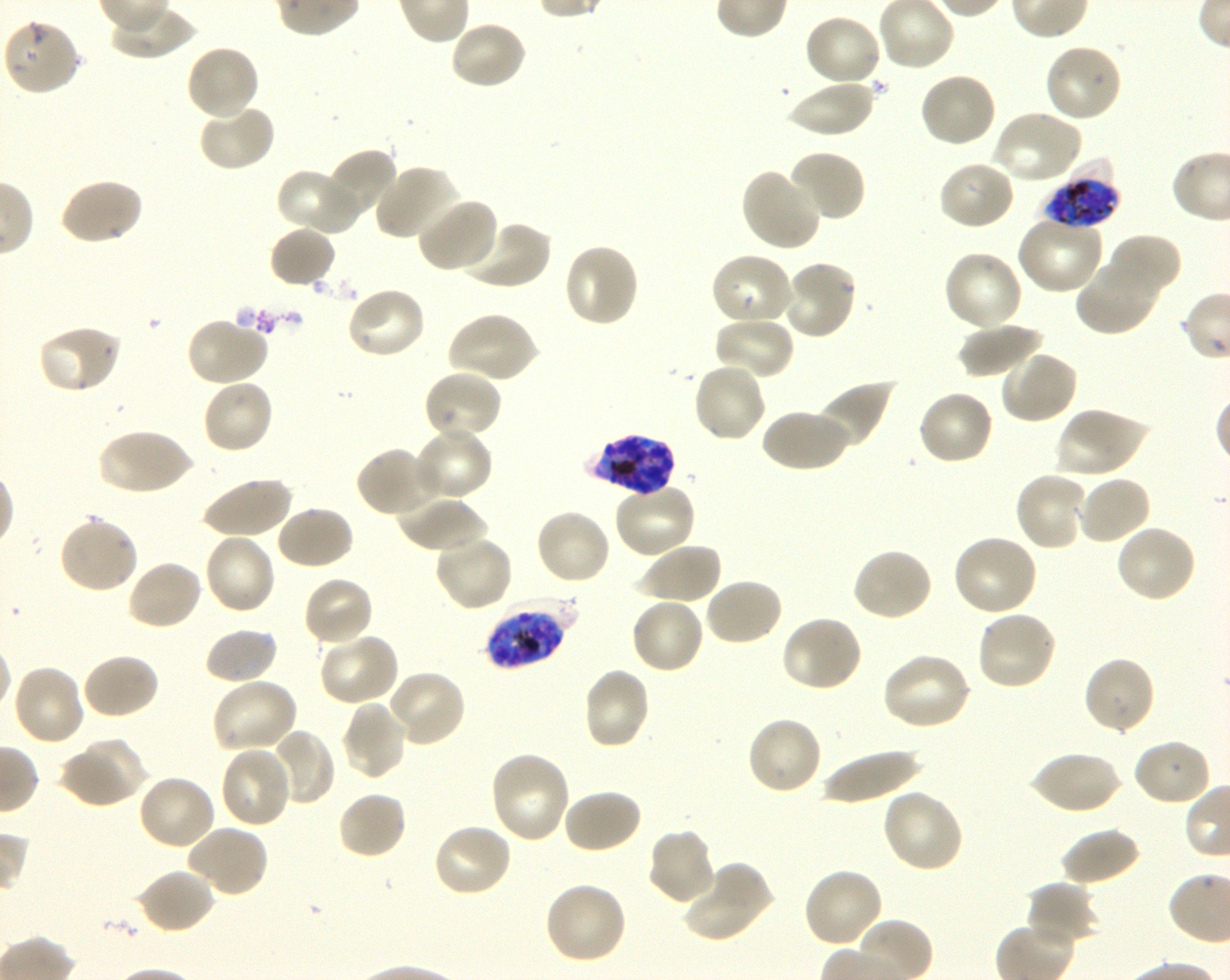

Approximate bounding boxes as {x1, y1, x2, y2} in pixels. Not every red blood cell is marked. A life-cycle stage — or a range of stages, where the recorded stages span more than one — follows each staged infected red blood cell.
Summary:
  - Locations of infected red blood cells: {1043, 167, 1120, 229} late trophozoite to late schizont; {587, 433, 675, 497} schizont; {483, 602, 571, 671} late trophozoite to late schizont
  - Locations of uninfected red blood cells: {803, 13, 883, 88}, {2, 17, 82, 97}, {448, 19, 528, 91}, {1043, 42, 1122, 122}, {185, 44, 260, 122}, {918, 72, 997, 149}, {785, 77, 876, 138}, {198, 105, 277, 173}, {991, 110, 1084, 187}, {324, 148, 399, 220}, {787, 150, 867, 223}, {936, 160, 1016, 232}, {374, 163, 460, 241}, {278, 167, 361, 236}, {739, 167, 825, 252}, {59, 177, 144, 246}, {414, 196, 498, 274}, {1015, 215, 1105, 296}, {458, 219, 552, 291}, {268, 225, 337, 289}, {1108, 234, 1182, 299}, {562, 242, 641, 328}, {942, 249, 1025, 332}, {709, 252, 794, 328}, {1075, 254, 1163, 337}, {780, 259, 858, 340}, {345, 286, 427, 361}, {446, 310, 539, 385}, {713, 315, 795, 380}, {185, 318, 270, 387}, {959, 321, 1045, 378}, {36, 324, 122, 394}, {999, 349, 1079, 424}, {691, 360, 767, 444}, {422, 369, 503, 442}, {201, 378, 275, 455}, {816, 378, 897, 450}, {916, 389, 994, 466}, {761, 407, 850, 473}, {1055, 407, 1146, 479}, {97, 427, 193, 496}, {413, 427, 493, 503}, {356, 446, 436, 518}, {1013, 470, 1089, 552}, {1075, 474, 1152, 546}, {200, 475, 292, 540}, {612, 481, 697, 559}, {395, 497, 489, 553}, {276, 505, 354, 570}, {534, 507, 613, 586}, {57, 514, 140, 593}, {1114, 523, 1198, 604}, {202, 532, 277, 615}, {434, 533, 514, 612}, {951, 534, 1038, 618}, {637, 542, 722, 606}, {851, 547, 934, 622}, {126, 558, 203, 631}, {302, 575, 375, 647}, {703, 577, 783, 647}, {629, 596, 705, 675}, {975, 609, 1058, 692}, {780, 614, 864, 693}, {203, 626, 278, 685}, {316, 632, 399, 706}, {881, 651, 973, 731}, {80, 652, 160, 720}, {1082, 655, 1157, 735}, {11, 663, 85, 747}, {581, 667, 652, 751}, {385, 669, 466, 748}, {210, 677, 299, 754}, {340, 699, 409, 781}, {745, 715, 824, 795}, {267, 728, 337, 807}, {1133, 737, 1213, 806}, {56, 743, 137, 809}, {219, 746, 293, 829}, {819, 746, 923, 805}, {1028, 750, 1122, 815}, {488, 751, 572, 844}, {137, 773, 217, 850}, {881, 787, 965, 874}, {562, 788, 643, 855}, {336, 790, 408, 861}, {431, 822, 514, 898}, {185, 825, 270, 900}, {1059, 826, 1141, 887}, {646, 829, 719, 905}, {682, 861, 774, 944}, {801, 865, 884, 948}, {136, 867, 217, 935}, {542, 881, 628, 966}, {1025, 881, 1099, 948}
  - Preparation: thin blood smear
  - Objective: 100x, oil immersion, numerical aperture 1.30
  - Image size: 1230×980 pixels
  - Culture: in-vitro P. falciparum strain 3D7, shaking
  - Stain: Giemsa
  - Field of view: single
  - Donor blood group: O+